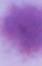

Micrograph. An erythrocyte is shown. Captured at 1000x magnification.